Classify this cell by malaria status.
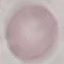
Uninfected.

image_type: cell patch, automatically extracted from a larger field of view and resized to 64 × 64 pixels
stain: Giemsa
preparation: thin blood film
capture: smartphone camera at the microscope eyepiece